State which parasite is depicted.
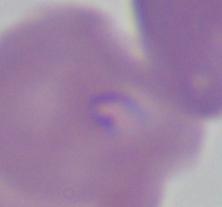
This is Babesia.

modality = micrograph
magnification = 1000x